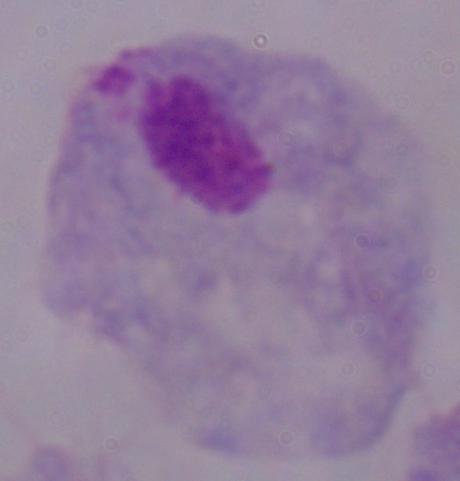

Micrograph. A trichomonad is seen. Captured at 1000x magnification.